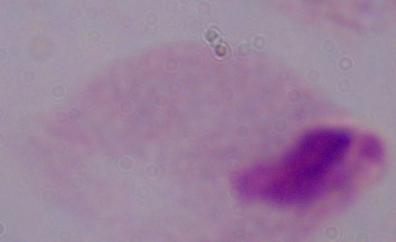
modality: photomicrograph
magnification: 1000x
identification: trichomonad